Classify this cell by malaria status.
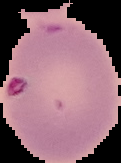

It is uninfected.

From a thin blood film. The area outside the segmented cell region is set to black. Image is 121×163 pixels.